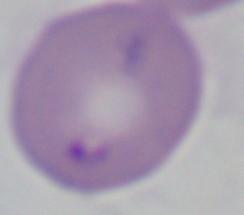
Summary:
  - Modality: micrograph
  - Identification: Babesia
  - Magnification: 1000x